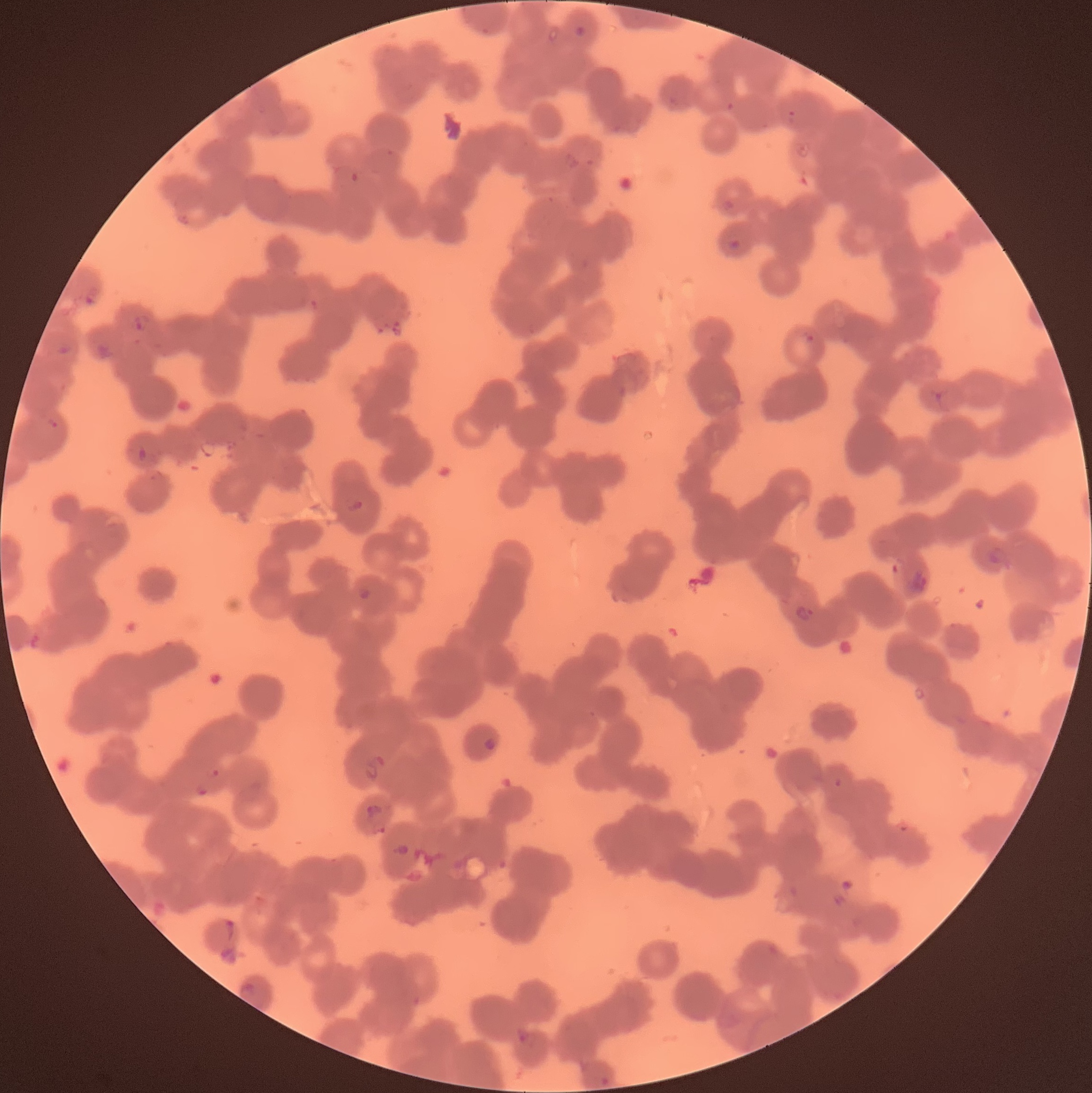 Approximate bounding boxes as named x1/y1/x2/y2 corners in pixels. Plasmodium parasite locations: (x1=574, y1=24, x2=587, y2=39), (x1=721, y1=196, x2=737, y2=211), (x1=727, y1=237, x2=742, y2=250), (x1=132, y1=315, x2=150, y2=332), (x1=46, y1=416, x2=60, y2=429), (x1=138, y1=445, x2=149, y2=463), (x1=346, y1=499, x2=363, y2=513), (x1=987, y1=544, x2=1008, y2=569), (x1=356, y1=585, x2=372, y2=601), (x1=794, y1=605, x2=816, y2=626), (x1=483, y1=738, x2=498, y2=751). Thin blood smear. Optical microscopy. The red blood cells show rouleaux formation. Image is 1092×1093 pixels.